Assess the morphology of the red blood cells.
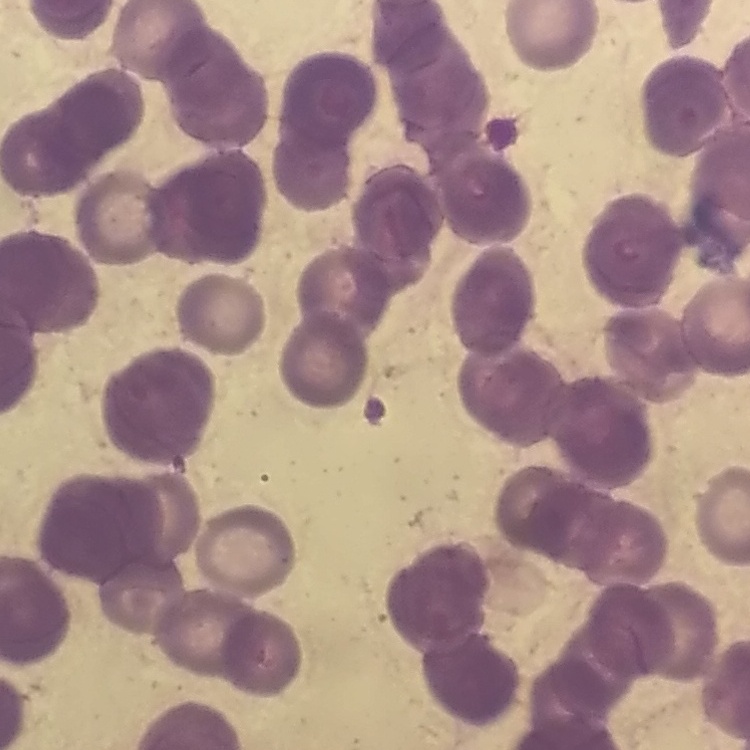

They show rouleaux formation.

Stained with either Field's or Giemsa. One tile cut from a larger photomicrograph. Thin blood smear.